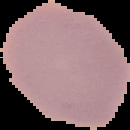
Summary:
  - Preparation: thin blood film
  - Malaria status: uninfected
  - Image size: 130×130 pixels
  - Image type: cell region segmented out of the field of view; surrounding area masked to black